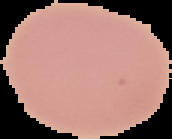 Result: no malaria parasites detected. Segmented cell region on a black background. From a thin blood film. Image is 172×139 pixels.